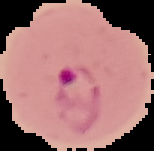
{
  "preparation": "thin blood film",
  "image_size": "154×151 pixels",
  "image_type": "segmented cell region on a black background",
  "malaria_status": "parasitized"
}